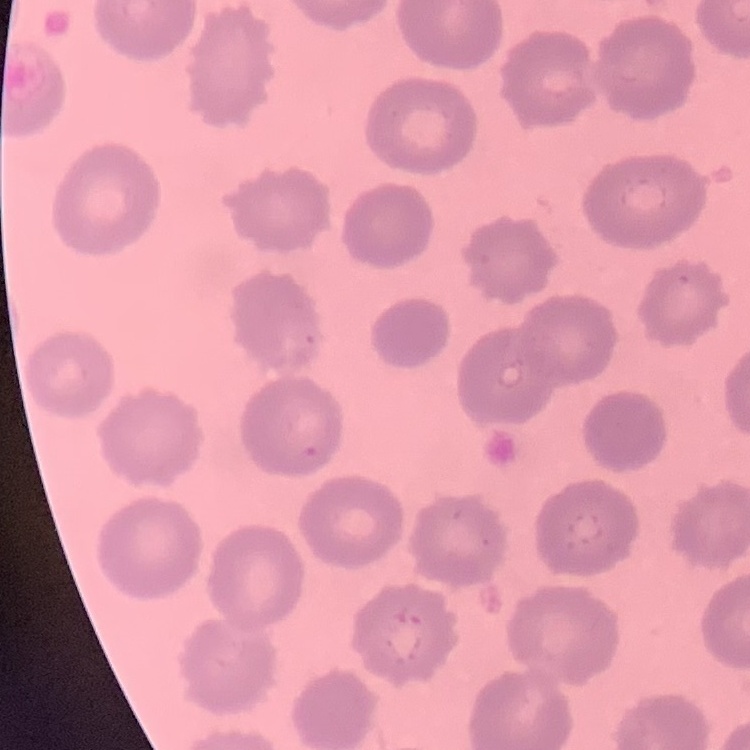
{
  "erythrocyte_morphology": "no rouleaux formation",
  "preparation": "thin peripheral smear",
  "image_type": "one tile cut from a larger photomicrograph",
  "stain": "Field's or Giemsa"
}